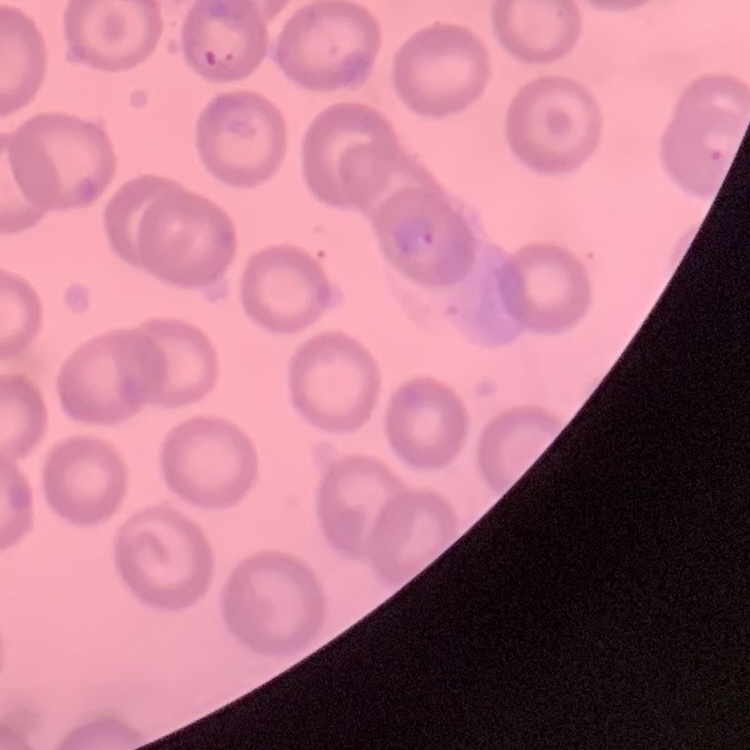 The red blood cells show no rouleaux formation. One tile cut from a larger photomicrograph. Thin blood smear. Stained with either Field's or Giemsa.